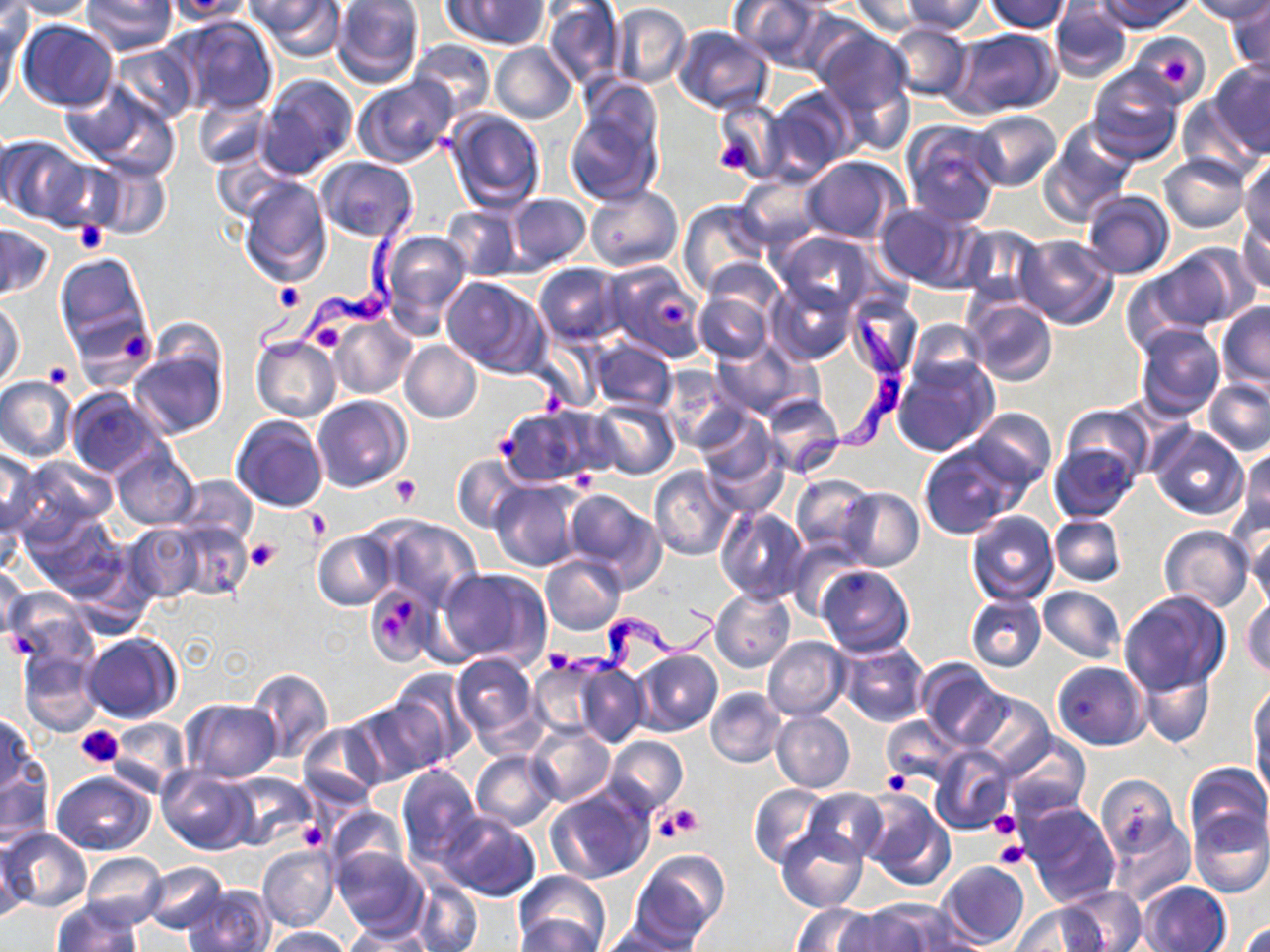

Summary:
  - Coordinate format: approximate bounding boxes as (x1, y1, x2, y2) in pixels
  - Trypanosoma brucei locations: (256, 200, 416, 362), (791, 311, 917, 504), (542, 605, 724, 689)
  - Platelet locations: (1160, 53, 1192, 84), (712, 133, 757, 176), (76, 220, 107, 254), (274, 281, 305, 311), (659, 299, 690, 330), (308, 319, 348, 354), (120, 328, 149, 360), (43, 361, 73, 387), (540, 387, 568, 416), (497, 434, 524, 458), (391, 474, 421, 505), (304, 508, 332, 542), (246, 537, 280, 572), (397, 600, 414, 625), (381, 613, 403, 639), (5, 632, 36, 657), (75, 726, 122, 769), (881, 770, 909, 794), (664, 804, 705, 839), (989, 807, 1021, 840), (299, 822, 327, 850), (993, 839, 1031, 869)
  - White blood cell locations: (573, 469, 597, 493)
  - Uninfected red blood cell locations: (5, 0, 96, 20), (80, 0, 179, 54), (247, 0, 343, 60), (331, 0, 424, 87), (446, 0, 548, 48), (729, 0, 827, 71), (901, 0, 990, 35), (984, 0, 1070, 32), (1098, 0, 1192, 32), (1188, 0, 1270, 24), (851, 1, 929, 37), (1049, 2, 1134, 83), (543, 3, 624, 87), (612, 3, 690, 88), (1226, 3, 1270, 79), (0, 4, 31, 62), (172, 14, 278, 116), (0, 19, 21, 115), (19, 20, 119, 113), (885, 23, 973, 100), (671, 25, 773, 114), (949, 27, 1062, 116), (813, 28, 914, 121), (1129, 32, 1211, 105), (409, 38, 494, 120), (109, 41, 199, 125), (492, 43, 577, 123), (1209, 59, 1270, 157), (1087, 67, 1184, 164), (256, 73, 358, 179), (353, 76, 459, 170), (63, 81, 180, 177), (764, 87, 858, 181), (193, 95, 273, 169), (1178, 95, 1264, 182), (712, 96, 785, 184), (564, 105, 661, 208), (444, 108, 545, 210), (968, 110, 1061, 192), (902, 119, 1003, 227), (1042, 120, 1137, 222), (2, 135, 91, 226), (210, 152, 288, 222), (1158, 154, 1250, 233), (799, 155, 907, 245), (315, 156, 420, 243), (1239, 157, 1269, 244), (86, 158, 172, 242), (736, 173, 822, 249), (238, 174, 331, 287), (584, 185, 681, 272), (1081, 189, 1175, 279), (503, 193, 589, 271), (583, 194, 770, 285), (678, 200, 772, 295), (875, 202, 977, 291), (442, 205, 523, 278), (1236, 216, 1270, 296), (0, 222, 55, 302), (957, 224, 1045, 307), (378, 228, 474, 336), (770, 230, 879, 314), (1015, 235, 1118, 329), (1145, 245, 1250, 333), (54, 251, 152, 361), (700, 257, 785, 329), (602, 260, 708, 362), (534, 263, 625, 347), (441, 276, 549, 378), (766, 278, 858, 366), (694, 290, 773, 364), (696, 291, 813, 399), (845, 295, 922, 381), (964, 297, 1058, 386), (0, 301, 26, 389), (1216, 302, 1270, 394), (329, 315, 416, 398), (905, 319, 993, 393), (1134, 322, 1225, 421), (251, 335, 341, 422), (589, 338, 677, 414), (399, 340, 482, 424), (711, 340, 805, 418), (128, 345, 226, 440), (892, 356, 998, 457), (660, 368, 749, 454), (0, 375, 76, 463), (1203, 377, 1270, 455), (67, 387, 167, 478), (760, 392, 845, 476), (311, 395, 411, 494), (589, 398, 679, 480), (498, 404, 612, 490), (1060, 404, 1153, 486), (968, 407, 1055, 492), (697, 411, 779, 492), (231, 416, 329, 514), (1148, 425, 1249, 520), (919, 441, 1023, 539), (1049, 442, 1141, 523), (110, 444, 200, 530), (1238, 447, 1270, 534), (0, 448, 44, 538), (14, 454, 117, 541), (452, 456, 528, 533), (650, 466, 738, 560), (175, 474, 258, 544), (789, 474, 874, 554), (489, 480, 586, 572), (561, 488, 665, 589), (837, 488, 923, 571), (716, 507, 808, 602), (28, 510, 129, 608), (966, 511, 1059, 605), (1050, 514, 1125, 587), (373, 517, 482, 610), (163, 519, 252, 602), (127, 522, 206, 602), (1246, 523, 1269, 612), (1158, 525, 1254, 612), (313, 530, 396, 609), (786, 538, 864, 620), (540, 554, 626, 635), (0, 561, 28, 642), (817, 564, 914, 657), (439, 566, 552, 670), (366, 586, 436, 667), (1039, 586, 1125, 663), (710, 587, 795, 673), (4, 590, 94, 665), (1118, 590, 1232, 697), (965, 593, 1046, 672), (1243, 595, 1270, 679), (83, 632, 181, 724), (763, 636, 848, 721), (836, 639, 930, 727), (18, 648, 103, 735), (632, 650, 722, 737), (450, 652, 541, 747), (571, 659, 647, 748), (917, 660, 1006, 751), (1052, 661, 1149, 750), (529, 662, 608, 739), (1138, 665, 1215, 750), (246, 667, 334, 764), (387, 669, 477, 765), (1250, 685, 1269, 777), (705, 686, 785, 769), (967, 690, 1052, 777), (346, 697, 446, 786), (181, 699, 281, 781), (772, 710, 855, 792), (0, 714, 39, 800), (881, 716, 962, 785), (106, 717, 190, 794), (297, 722, 385, 808), (526, 724, 614, 806), (1001, 731, 1091, 818), (605, 735, 689, 816), (929, 746, 1012, 835), (471, 751, 559, 831), (0, 759, 53, 849), (1184, 763, 1269, 848), (397, 764, 481, 865), (158, 767, 254, 854), (52, 771, 155, 856), (223, 771, 314, 850), (1097, 774, 1180, 858), (748, 785, 829, 868), (544, 786, 654, 885), (802, 788, 888, 864), (860, 791, 955, 891), (1018, 801, 1120, 909), (324, 805, 407, 880), (1189, 810, 1270, 899), (437, 812, 540, 901), (1106, 812, 1194, 905), (777, 827, 867, 913), (1122, 827, 1209, 945), (2, 828, 91, 912), (1, 832, 30, 925), (258, 845, 338, 932), (331, 845, 430, 938), (635, 849, 729, 943), (82, 852, 167, 929), (937, 860, 1030, 949), (142, 861, 228, 935), (515, 869, 610, 951), (413, 881, 482, 952), (1137, 881, 1231, 951), (185, 883, 275, 952), (1060, 887, 1146, 951), (53, 900, 141, 951), (865, 900, 972, 950), (792, 903, 881, 951), (1011, 903, 1106, 950), (835, 908, 930, 952), (515, 915, 603, 951), (600, 917, 698, 951), (1240, 921, 1270, 952), (343, 925, 438, 951), (263, 926, 353, 952)
  - Slide-level diagnosis: Trypanosoma brucei
  - Magnification: 1000x
  - Field of view: one of a larger specimen
  - Modality: light microscopy
  - Stain: May-Grünwald-Giemsa
  - Preparation: thin blood smear
  - Image size: 1270×952 pixels